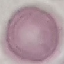
Summary:
  - Result: negative for malaria parasites
  - Image type: automatically extracted cell patch, resized to 64 × 64 pixels
  - Preparation: thin smear
  - Capture: smartphone through the microscope eyepiece
  - Stain: Giemsa